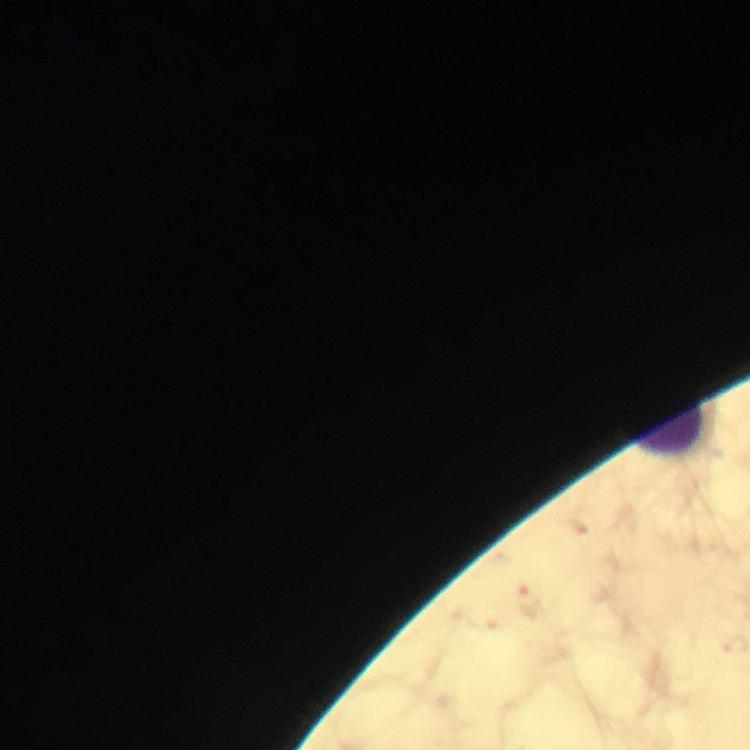

Approximate centers as {x, y} in pixels.
Summary:
  - Leukocyte locations: {670, 430}
  - Stain: Giemsa
  - Cropped from: a single field of view
  - Magnification: 100x
  - Plasmodium parasites: none detected
  - Preparation: thick blood smear
  - Capture: smartphone mounted on the microscope
  - Image size: 750×750 pixels
  - Immersion oil: used
  - Context: from a malaria diagnostic workup